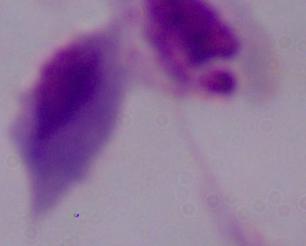
Photomicrograph. 1000x magnification. A trichomonad is seen.